Report the malaria status of this cell.
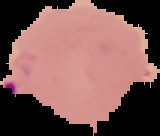
Parasitized.

Image is 160×136 pixels. Segmented cell region on a black background. From a thin blood film.